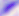
magnification = 400x
identification = Toxoplasma gondii
modality = micrograph